Name the parasite shown.
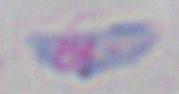

Toxoplasma gondii.

magnification = 1000x
modality = micrograph